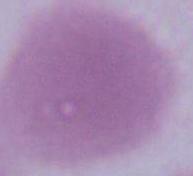
Micrograph. An erythrocyte is shown. Captured at 1000x magnification.